Point out each Plasmodium parasite.
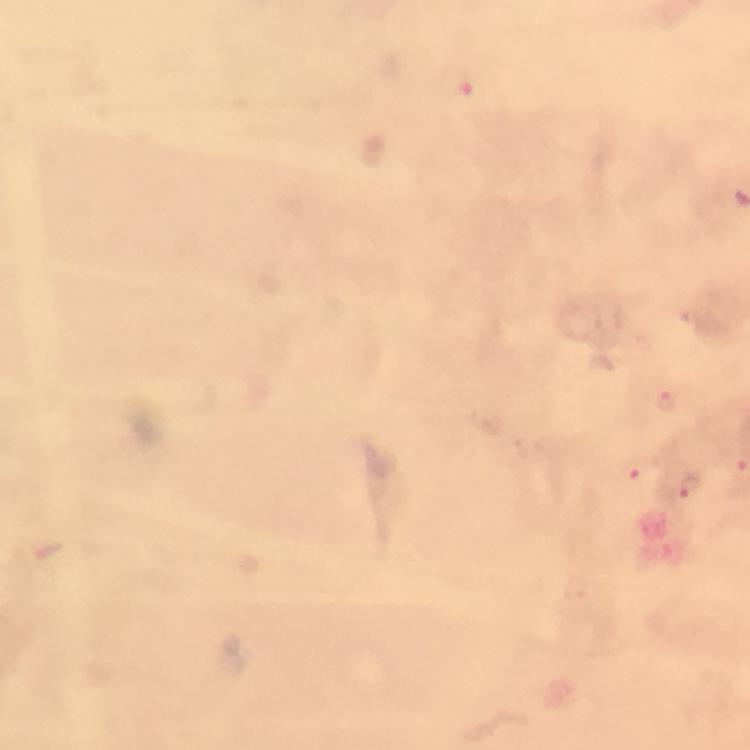

Approximate centers as [x, y] in pixels.
Plasmodium parasites: [462, 87], [668, 403], [637, 468], [685, 487].

preparation = thick blood film
cropped from = one field of view
context = from a diagnostic examination for malaria
magnification = 100x
stain = Giemsa
immersion oil = used
capture = smartphone photograph through a microscope
image size = 750×750 pixels